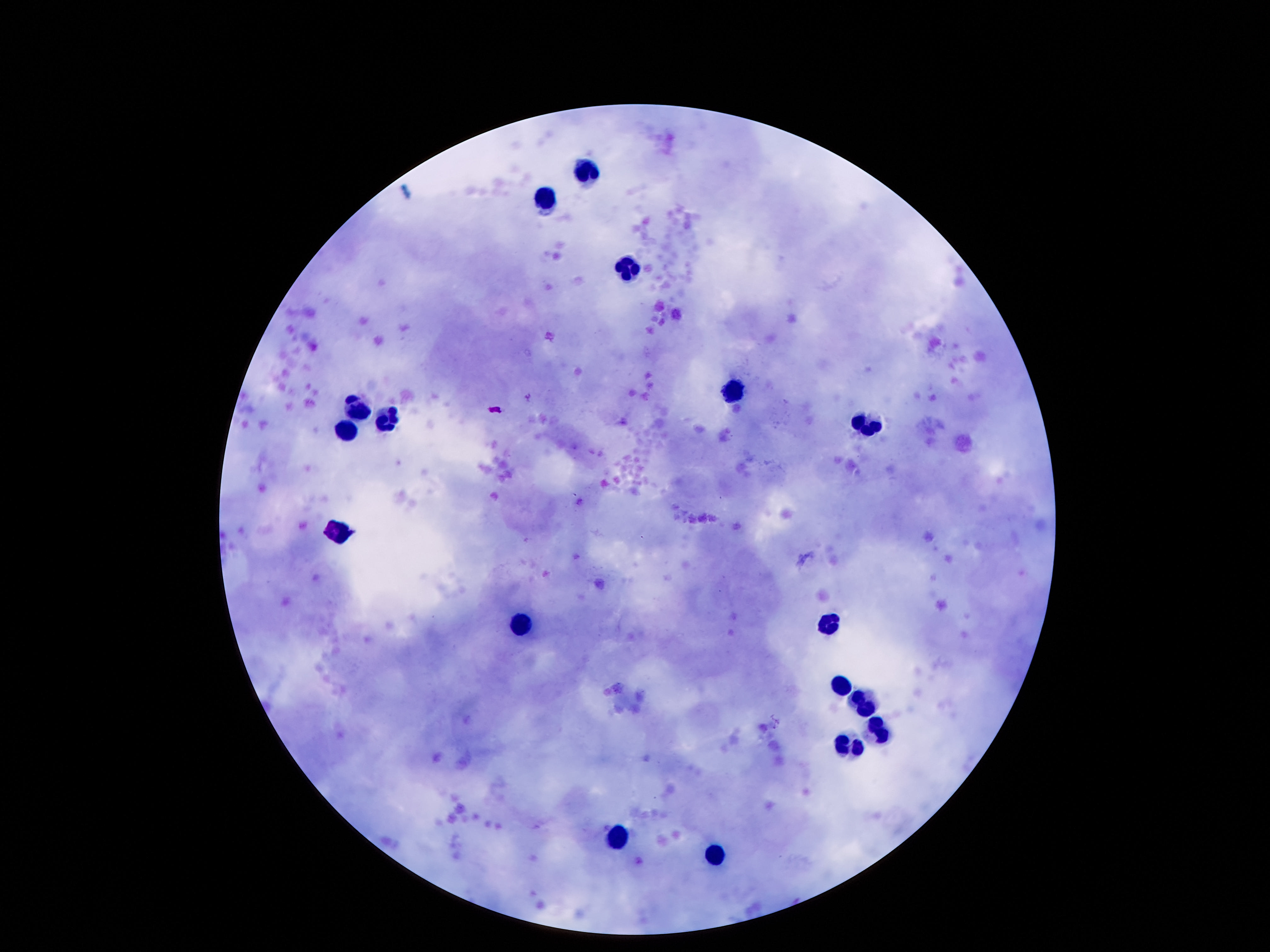

Approximate centers as [x, y] in pixels.
Summary:
  - Leukocyte locations: [587, 171], [547, 197], [628, 272], [739, 392], [354, 406], [386, 418], [871, 425], [350, 430], [335, 533], [830, 622], [520, 629], [839, 682], [863, 704], [878, 730], [851, 747], [619, 838], [717, 855]
  - Magnification: 100x
  - Field of view: one from this slide
  - Patient malaria status: not infected
  - Preparation: thick blood film
  - Image size: 1270×952 pixels
  - Capture: smartphone camera through the microscope eyepiece
  - Stain: Giemsa